Give a bounding box for every parasitised red blood cell, every trophozoite, every gametocyte, every leukocyte, and every artifact (platelet-like body, stain precipitate, or debris).
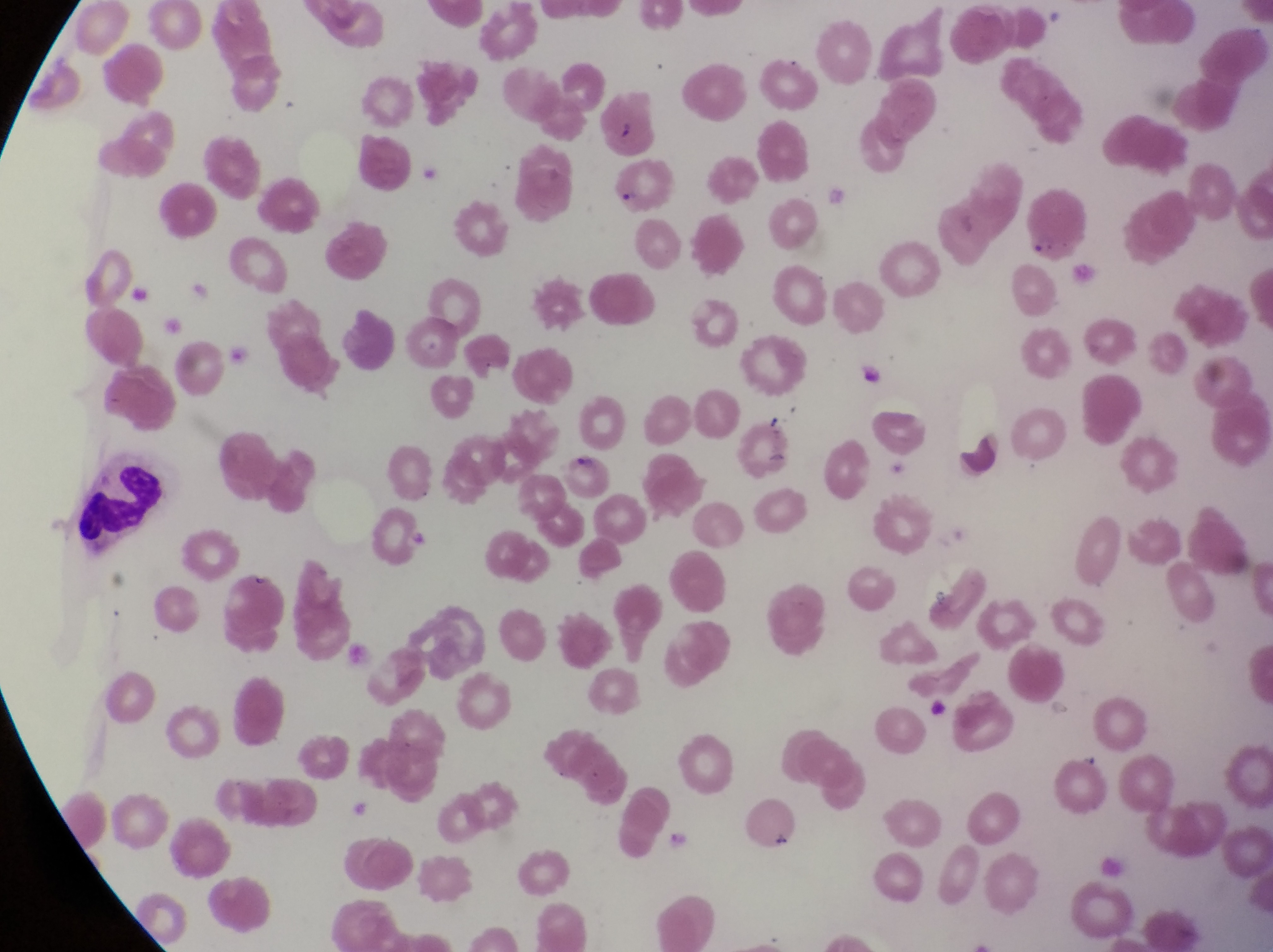

Approximate bounding boxes as (left, top, right, bottom) in pixels.
Parasitised red blood cells: (604, 155, 679, 212).
Leukocytes: (70, 449, 172, 544).
Artifacts (platelet-like body, stain precipitate, or debris): (861, 359, 891, 389), (956, 429, 1008, 469).

preparation = thin blood smear
magnification = 1000x
capture = smartphone photograph through the eyepiece of an Olympus CX-23 microscope
image size = 1273×952 pixels
country = Uganda
field of view = single